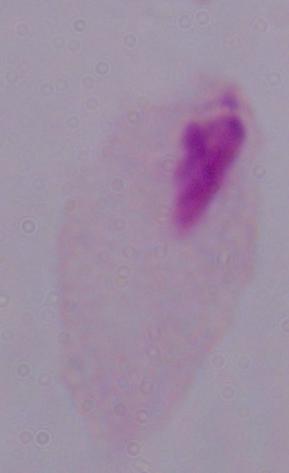
identification = trichomonad
modality = micrograph
magnification = 1000x